Classify this cell by malaria status.
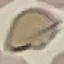
It is uninfected.

Summary:
  - Image type: cell patch, automatically extracted from a larger field of view and resized to 64 × 64 pixels
  - Capture: smartphone camera at the microscope eyepiece
  - Stain: Giemsa
  - Preparation: thin smear